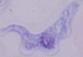
magnification = 1000x
modality = micrograph
identification = trypanosome